Assess this cell for malaria.
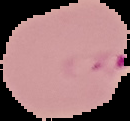
Parasitized.

Summary:
  - Preparation: thin blood film
  - Image type: segmented cell region on a black background
  - Image size: 130×121 pixels